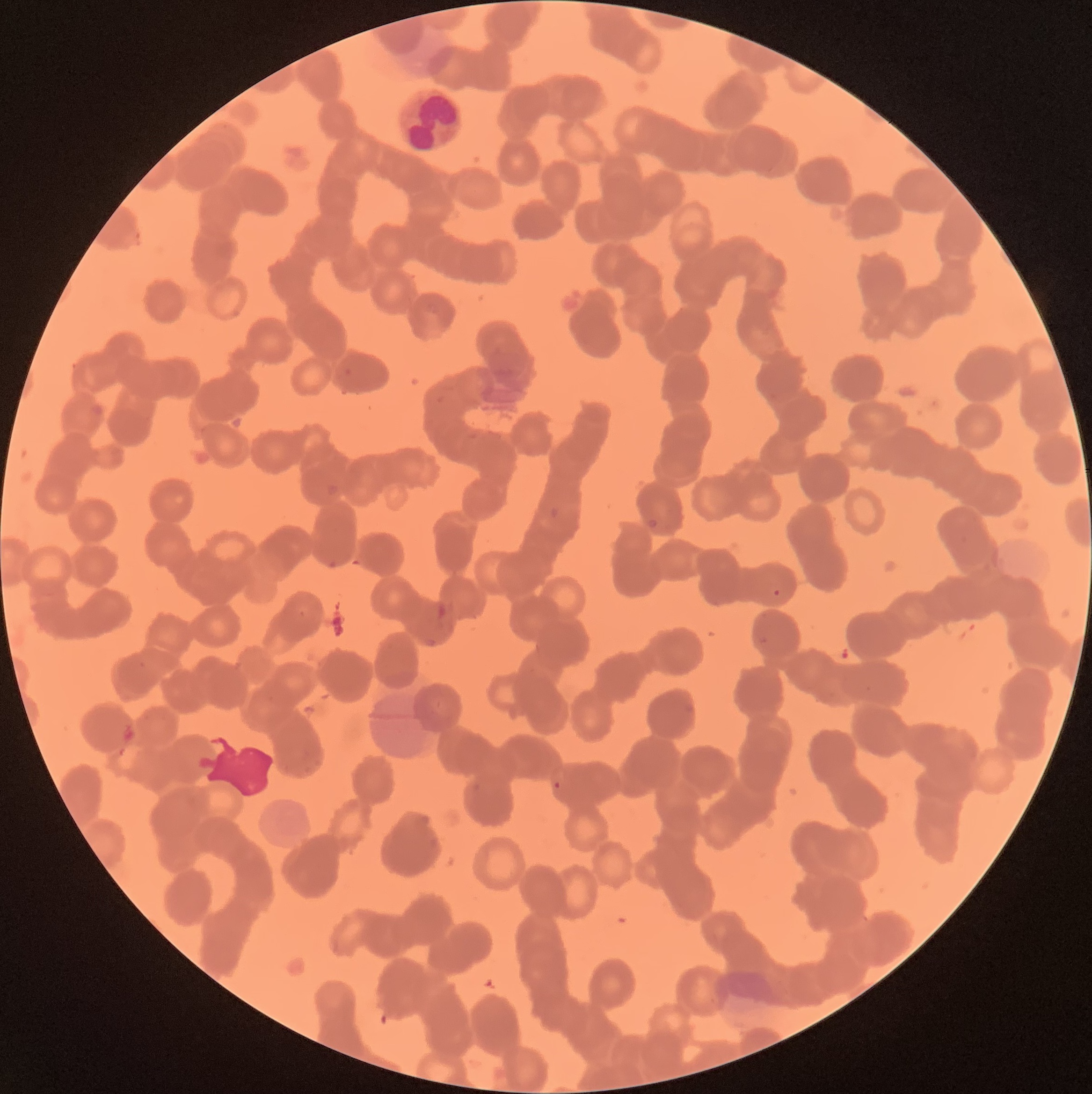

{
  "plasmodium_parasite_locations": "approximate bounding boxes as named x1/y1/x2/y2 corners in pixels: (x1=326, y1=483, x2=340, y2=496), (x1=547, y1=507, x2=561, y2=520), (x1=646, y1=519, x2=659, y2=528), (x1=327, y1=560, x2=338, y2=568), (x1=770, y1=588, x2=783, y2=599), (x1=757, y1=635, x2=769, y2=645), (x1=421, y1=636, x2=439, y2=647), (x1=864, y1=685, x2=873, y2=693), (x1=553, y1=781, x2=562, y2=789)",
  "red_blood_cell_morphology": "rouleaux formation",
  "image_size": "1092×1094 pixels",
  "modality": "optical microscopy",
  "preparation": "thin blood smear",
  "white_blood_cell_locations": "approximate bounding boxes as named x1/y1/x2/y2 corners in pixels: (x1=395, y1=86, x2=465, y2=157)"
}